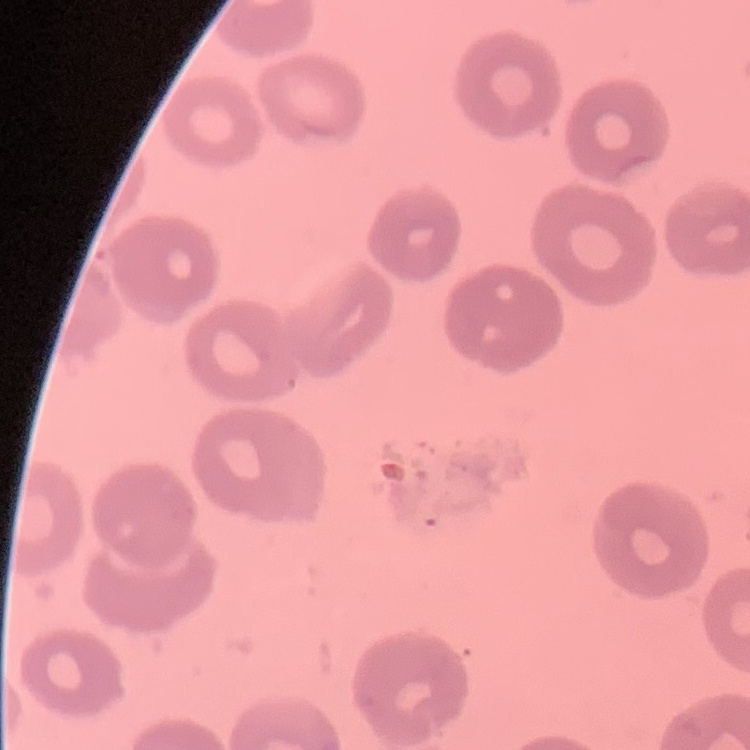

Summary:
  - Erythrocyte morphology: no rouleaux formation
  - Image type: square crop of a larger photomicrograph
  - Stain: Field's or Giemsa
  - Preparation: thin blood film